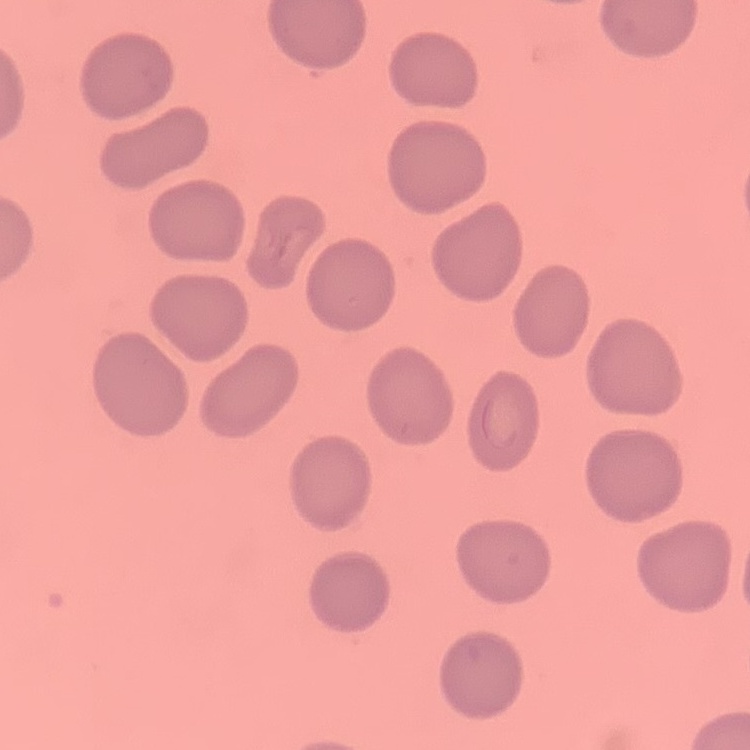
The erythrocytes exhibit no rouleaux formation. Thin peripheral smear. Square crop of a larger photomicrograph. Field's or Giemsa stain.